State which cell type is depicted.
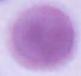

This is an erythrocyte.

magnification = 1000x
modality = photomicrograph